Assess the morphology of the erythrocytes.
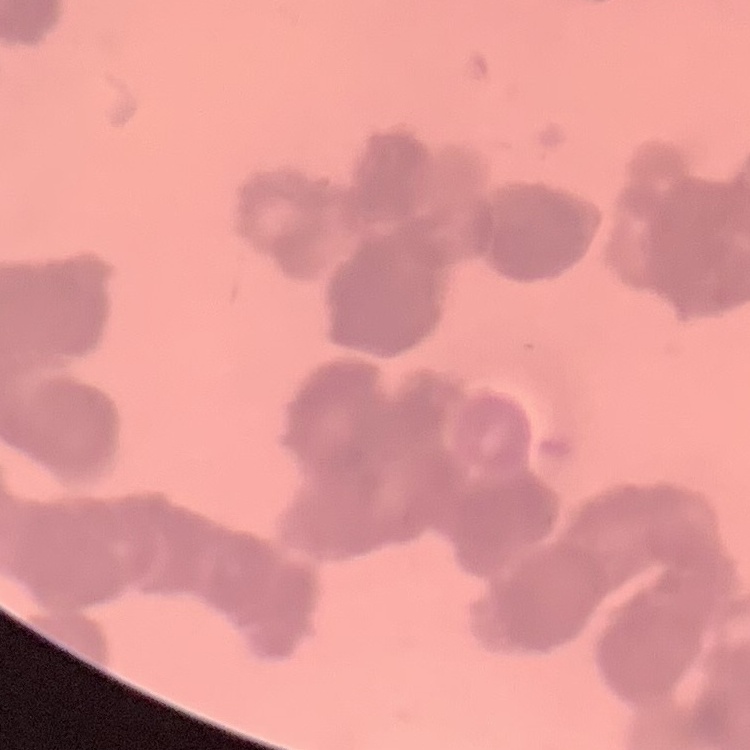
Rouleaux formation.

image type = one tile cut from a larger photomicrograph
preparation = thin blood smear
stain = Field's or Giemsa